Evaluate for parasitized red blood cells.
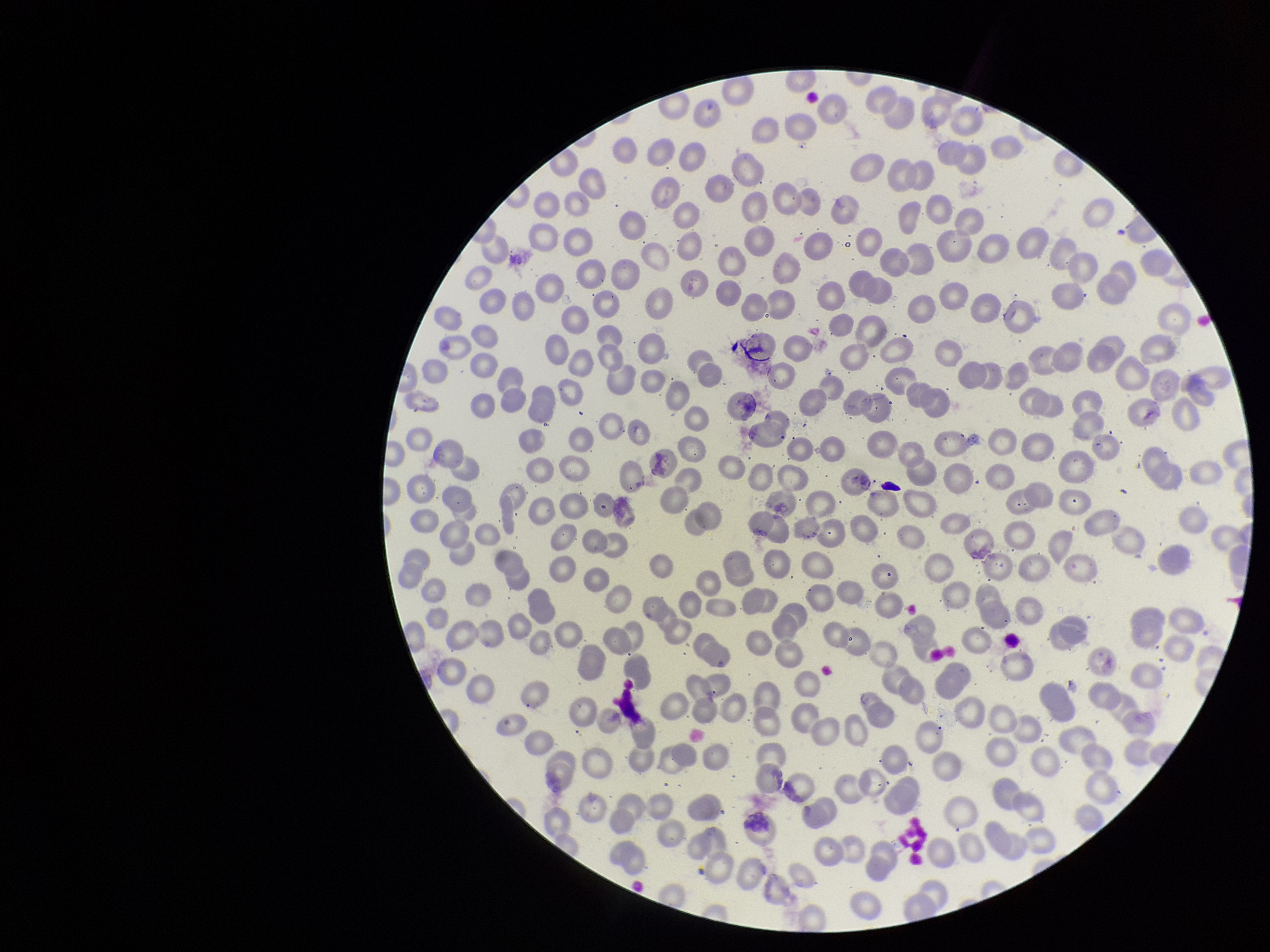
None detected.

red_blood_cell_count: 240
stain: Giemsa
field_of_view: single
parasitized_red_blood_cell_count: 0
image_size: 1270×952 pixels
patient_malaria_status: negative
capture: smartphone photograph through the microscope eyepiece
preparation: thin smear